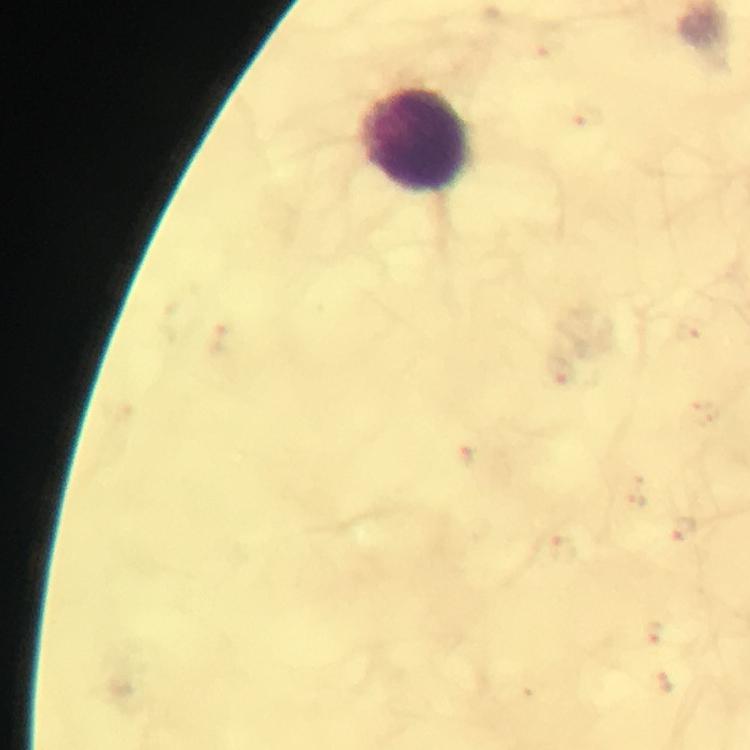
Approximate centers as {x, y} in pixels.
Summary:
  - Leukocyte locations: {415, 143}
  - Preparation: thick smear
  - Immersion oil: applied
  - Cropped from: one field of view
  - Plasmodium parasites: none detected
  - Image size: 750×750 pixels
  - Magnification: 100x
  - Stain: Giemsa
  - Capture: smartphone mounted on the microscope
  - Context: from a malaria diagnostic workup